Identify the blood parasite species.
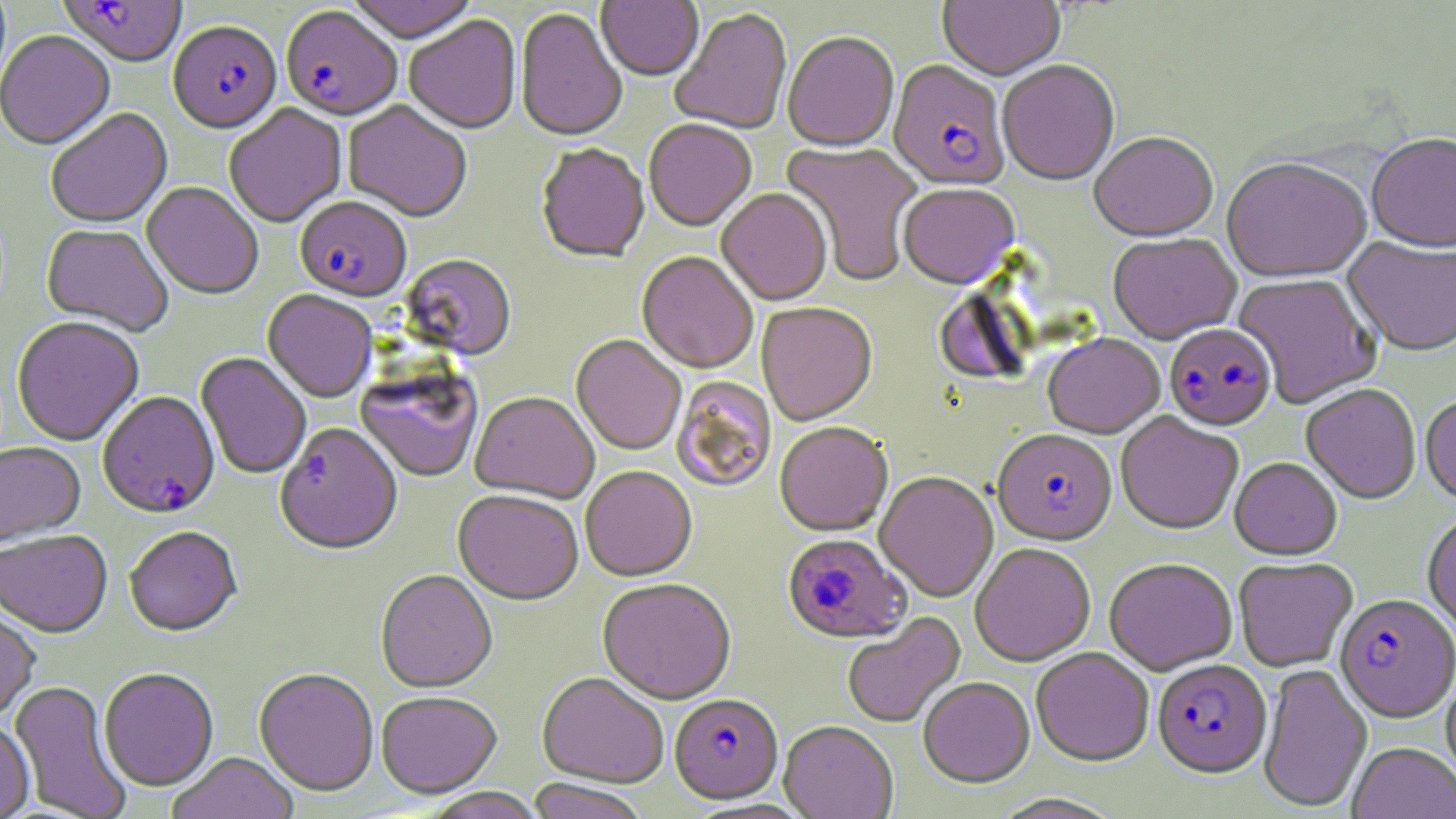
Plasmodium falciparum.

{
  "image_size": "1456×819 pixels",
  "uninfected_red_blood_cell_locations": "approximate bounding boxes as named x1/y1/x2/y2 corners in pixels: (x1=344, y1=0, x2=480, y2=46), (x1=938, y1=0, x2=1065, y2=84), (x1=596, y1=1, x2=704, y2=84), (x1=515, y1=9, x2=628, y2=144), (x1=670, y1=9, x2=793, y2=136), (x1=404, y1=17, x2=522, y2=136), (x1=0, y1=32, x2=115, y2=153), (x1=783, y1=34, x2=899, y2=154), (x1=997, y1=62, x2=1120, y2=188), (x1=342, y1=102, x2=472, y2=224), (x1=224, y1=105, x2=347, y2=230), (x1=46, y1=110, x2=172, y2=230), (x1=644, y1=121, x2=757, y2=234), (x1=1089, y1=134, x2=1218, y2=245), (x1=1366, y1=135, x2=1456, y2=256), (x1=780, y1=141, x2=923, y2=287), (x1=536, y1=146, x2=650, y2=265), (x1=1222, y1=161, x2=1372, y2=286), (x1=141, y1=184, x2=264, y2=301), (x1=898, y1=185, x2=1020, y2=292), (x1=716, y1=190, x2=832, y2=307), (x1=41, y1=226, x2=173, y2=337), (x1=1108, y1=235, x2=1242, y2=347), (x1=1342, y1=238, x2=1456, y2=359), (x1=636, y1=253, x2=758, y2=375), (x1=401, y1=255, x2=517, y2=362), (x1=1232, y1=274, x2=1382, y2=410), (x1=262, y1=291, x2=378, y2=405), (x1=757, y1=304, x2=878, y2=427), (x1=11, y1=318, x2=144, y2=448), (x1=571, y1=336, x2=686, y2=456), (x1=1043, y1=336, x2=1165, y2=441), (x1=195, y1=353, x2=311, y2=480), (x1=355, y1=373, x2=482, y2=485), (x1=671, y1=377, x2=777, y2=493), (x1=1300, y1=386, x2=1421, y2=506), (x1=470, y1=394, x2=598, y2=506), (x1=1419, y1=398, x2=1456, y2=508), (x1=1115, y1=413, x2=1243, y2=536), (x1=774, y1=424, x2=893, y2=538), (x1=0, y1=444, x2=85, y2=547), (x1=1230, y1=459, x2=1342, y2=562), (x1=580, y1=467, x2=697, y2=584), (x1=875, y1=473, x2=998, y2=603), (x1=452, y1=491, x2=583, y2=608), (x1=1422, y1=514, x2=1456, y2=638), (x1=124, y1=529, x2=243, y2=639), (x1=0, y1=532, x2=113, y2=640), (x1=970, y1=544, x2=1095, y2=668), (x1=1234, y1=559, x2=1357, y2=672), (x1=1104, y1=561, x2=1238, y2=676), (x1=375, y1=571, x2=497, y2=695), (x1=597, y1=580, x2=736, y2=707), (x1=0, y1=608, x2=41, y2=724), (x1=842, y1=612, x2=966, y2=729), (x1=1031, y1=649, x2=1154, y2=769), (x1=1257, y1=664, x2=1373, y2=812), (x1=100, y1=669, x2=219, y2=793), (x1=254, y1=670, x2=379, y2=799), (x1=1441, y1=671, x2=1456, y2=792), (x1=537, y1=674, x2=668, y2=790), (x1=918, y1=678, x2=1035, y2=789), (x1=8, y1=681, x2=132, y2=819), (x1=376, y1=693, x2=502, y2=800), (x1=0, y1=719, x2=34, y2=819), (x1=779, y1=723, x2=898, y2=819), (x1=1348, y1=743, x2=1456, y2=819), (x1=167, y1=754, x2=300, y2=819), (x1=526, y1=780, x2=649, y2=819), (x1=420, y1=788, x2=548, y2=819)",
  "field_of_view": "single",
  "modality": "light microscopy",
  "stain": "May-Grünwald-Giemsa",
  "preparation": "thin blood smear",
  "plasmodium_falciparum_infected_red_blood_cell_locations": "approximate bounding boxes as named x1/y1/x2/y2 corners in pixels: (x1=58, y1=1, x2=187, y2=70), (x1=281, y1=8, x2=403, y2=125), (x1=169, y1=23, x2=282, y2=136), (x1=888, y1=62, x2=1009, y2=194), (x1=295, y1=199, x2=411, y2=304), (x1=1164, y1=325, x2=1277, y2=434), (x1=98, y1=393, x2=220, y2=521), (x1=275, y1=426, x2=403, y2=559), (x1=992, y1=432, x2=1117, y2=549), (x1=782, y1=535, x2=911, y2=645), (x1=1334, y1=596, x2=1456, y2=726), (x1=1152, y1=660, x2=1272, y2=780), (x1=669, y1=695, x2=783, y2=806)",
  "magnification": "1000x"
}